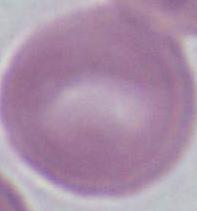
modality = photomicrograph
identification = red blood cell
magnification = 1000x